Locate every Plasmodium parasite.
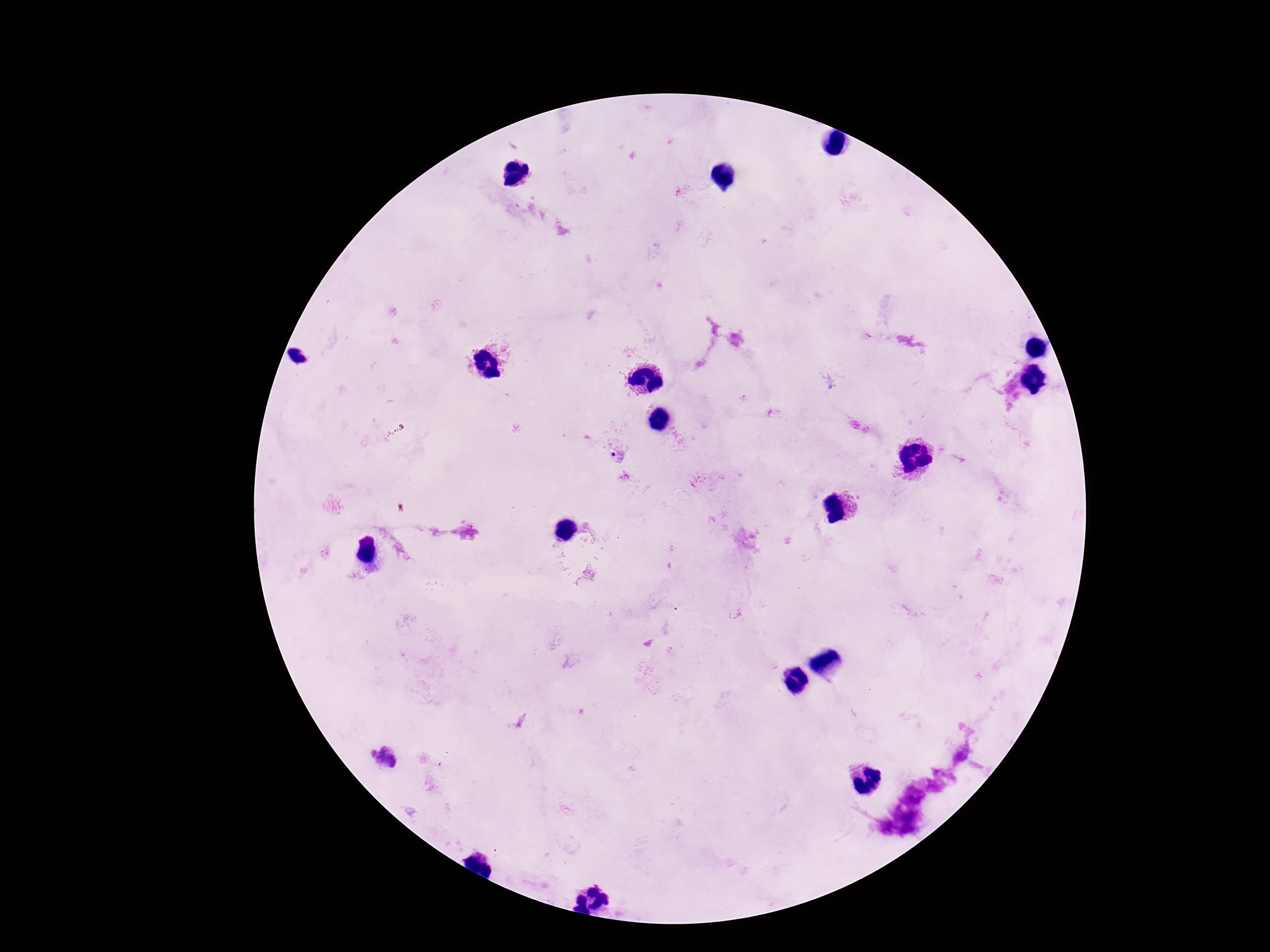

Approximate centers as (x, y) in pixels.
Plasmodium parasites: (617, 456), (384, 757).

Summary:
  - Stain: Giemsa
  - Magnification: 100x
  - Preparation: thick blood film
  - Patient malaria status: infected
  - Capture: smartphone camera through the microscope eyepiece
  - Field of view: one from this slide
  - Image size: 1270×952 pixels